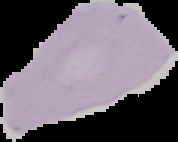
Summary:
  - Malaria status: uninfected
  - Image type: segmented cell region on a black background
  - Preparation: thin blood film
  - Image size: 178×142 pixels